Outline each Plasmodium ovale-infected red blood cell.
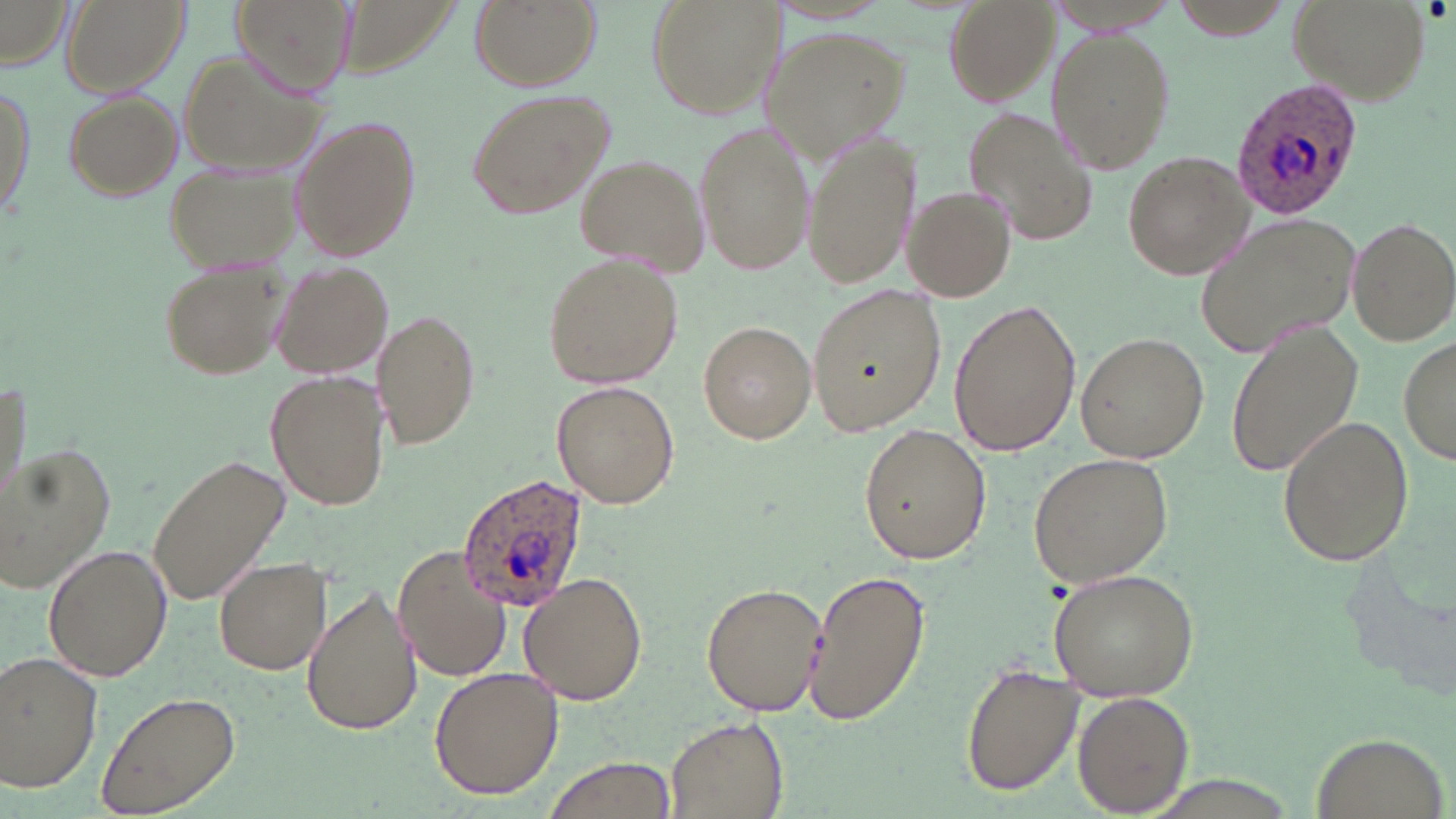

Approximate bounding boxes as (x1,y1)-(x2,y2) corner pairs in pixels.
Plasmodium ovale-infected red blood cells: (1227,72)-(1364,218), (457,475)-(591,615).

Summary:
  - Uninfected red blood cell locations: (60,0)-(186,97), (234,0)-(357,100), (467,0)-(600,92), (646,0)-(779,118), (941,0)-(1058,104), (1287,0)-(1431,107), (1161,1)-(1301,38), (0,2)-(71,66), (760,26)-(913,161), (1048,26)-(1175,176), (175,50)-(327,177), (1,76)-(36,233), (463,86)-(616,219), (58,87)-(184,203), (964,106)-(1100,247), (290,113)-(424,262), (693,119)-(816,278), (806,133)-(916,290), (1121,150)-(1257,280), (575,155)-(708,274), (163,162)-(304,273), (903,185)-(1017,303), (1196,210)-(1364,359), (1347,216)-(1456,347), (542,252)-(681,389), (155,258)-(293,384), (272,263)-(394,377), (807,285)-(946,434), (947,297)-(1082,458), (372,308)-(481,448), (697,321)-(815,442), (1228,321)-(1365,477), (1076,331)-(1207,464), (1398,336)-(1455,466), (0,372)-(31,513), (266,372)-(388,513), (549,380)-(680,508), (1277,414)-(1414,568), (857,424)-(991,565), (0,441)-(116,591), (147,451)-(290,607), (1030,451)-(1173,586), (394,542)-(515,683), (44,543)-(171,682), (213,557)-(331,675), (804,567)-(930,726), (1047,568)-(1199,700), (519,573)-(648,705), (703,581)-(827,719), (301,585)-(420,734), (2,651)-(104,794), (961,661)-(1082,796), (428,667)-(564,799), (1075,690)-(1195,816), (96,691)-(240,817), (665,716)-(787,818), (1312,730)-(1444,817), (539,755)-(677,819)
  - Slide-level diagnosis: Plasmodium ovale
  - Modality: optical microscopy
  - Preparation: thin blood film
  - Magnification: 1000x
  - Stain: May-Grünwald-Giemsa
  - Image size: 1456×819 pixels
  - Field of view: one of a larger specimen